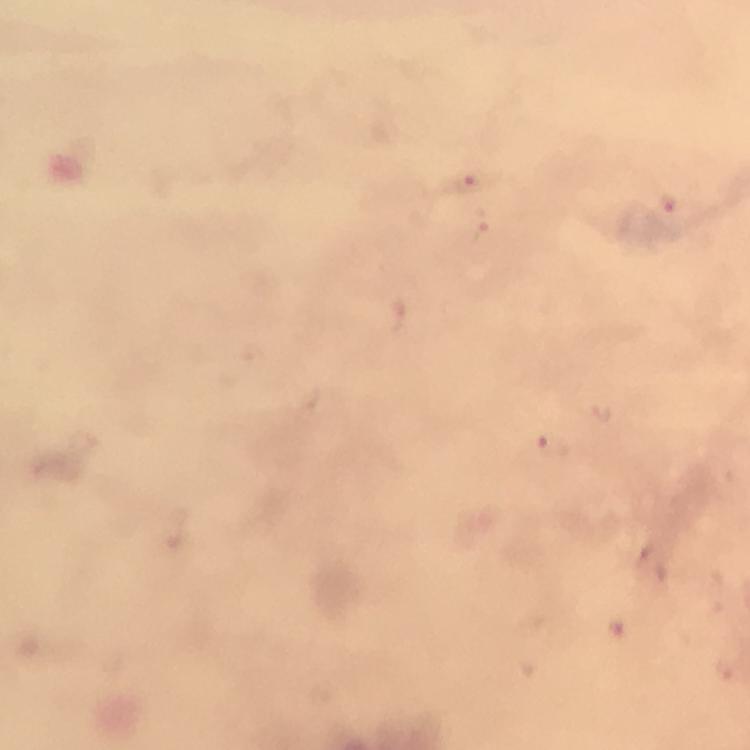
Approximate object centers, in pixels from the top-left corner. Plasmodium parasite locations: (x=468, y=184), (x=668, y=202), (x=602, y=415), (x=549, y=446). Giemsa stain. Photographed with a smartphone mounted on the microscope. Thick smear. Immersion oil applied. From a malaria diagnostic workup. A crop from one field of view. Image is 750×750 pixels. 100x magnification.